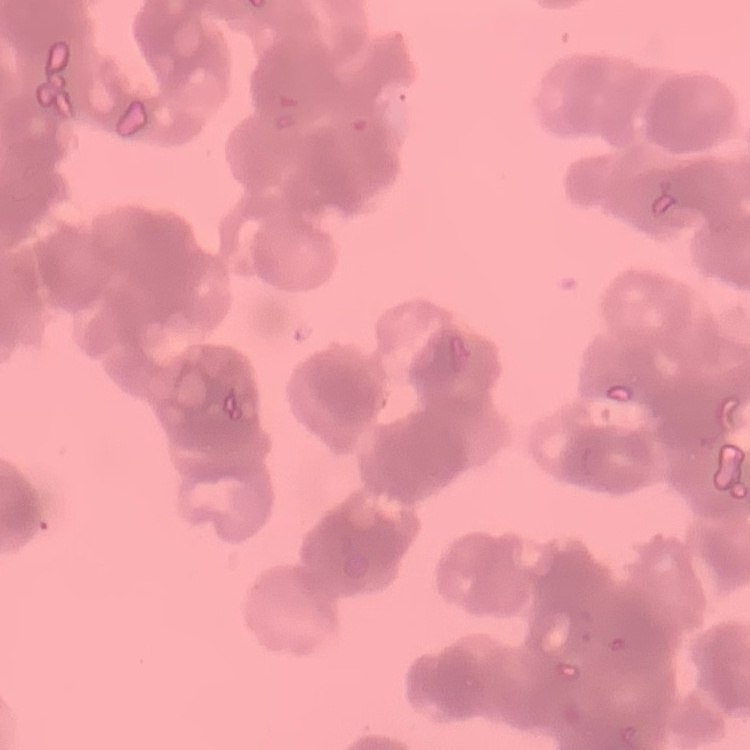

Summary:
  - Red blood cell morphology: rouleaux formation
  - Image type: one tile cut from a larger photomicrograph
  - Stain: Field's or Giemsa
  - Preparation: thin blood smear